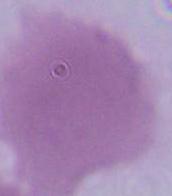 Photomicrograph. An erythrocyte is seen. Captured at 1000x magnification.